Describe the morphology of the erythrocytes.
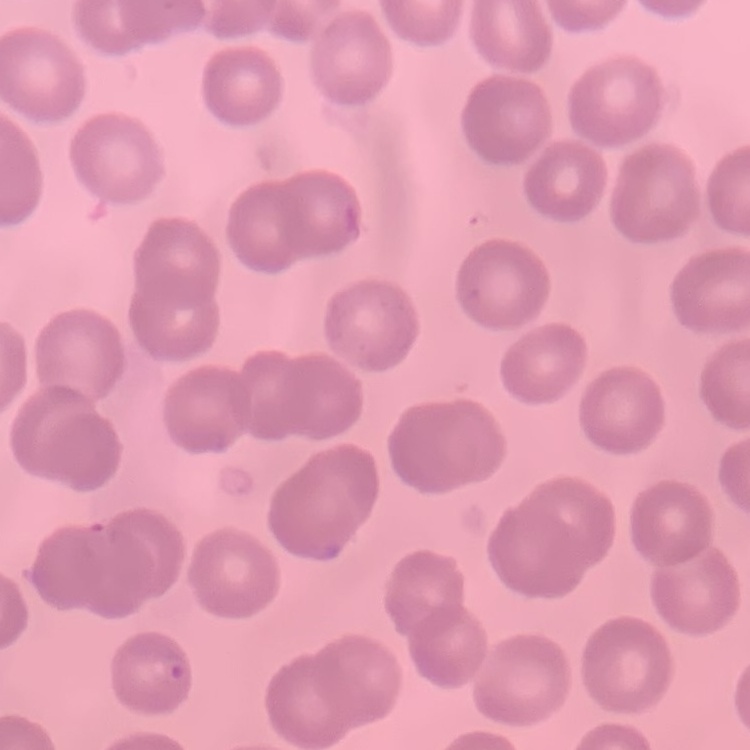
No rouleaux formation.

Summary:
  - Preparation: thin blood smear
  - Stain: Field's or Giemsa
  - Image type: one tile cut from a larger photomicrograph